Identify the blood parasite species.
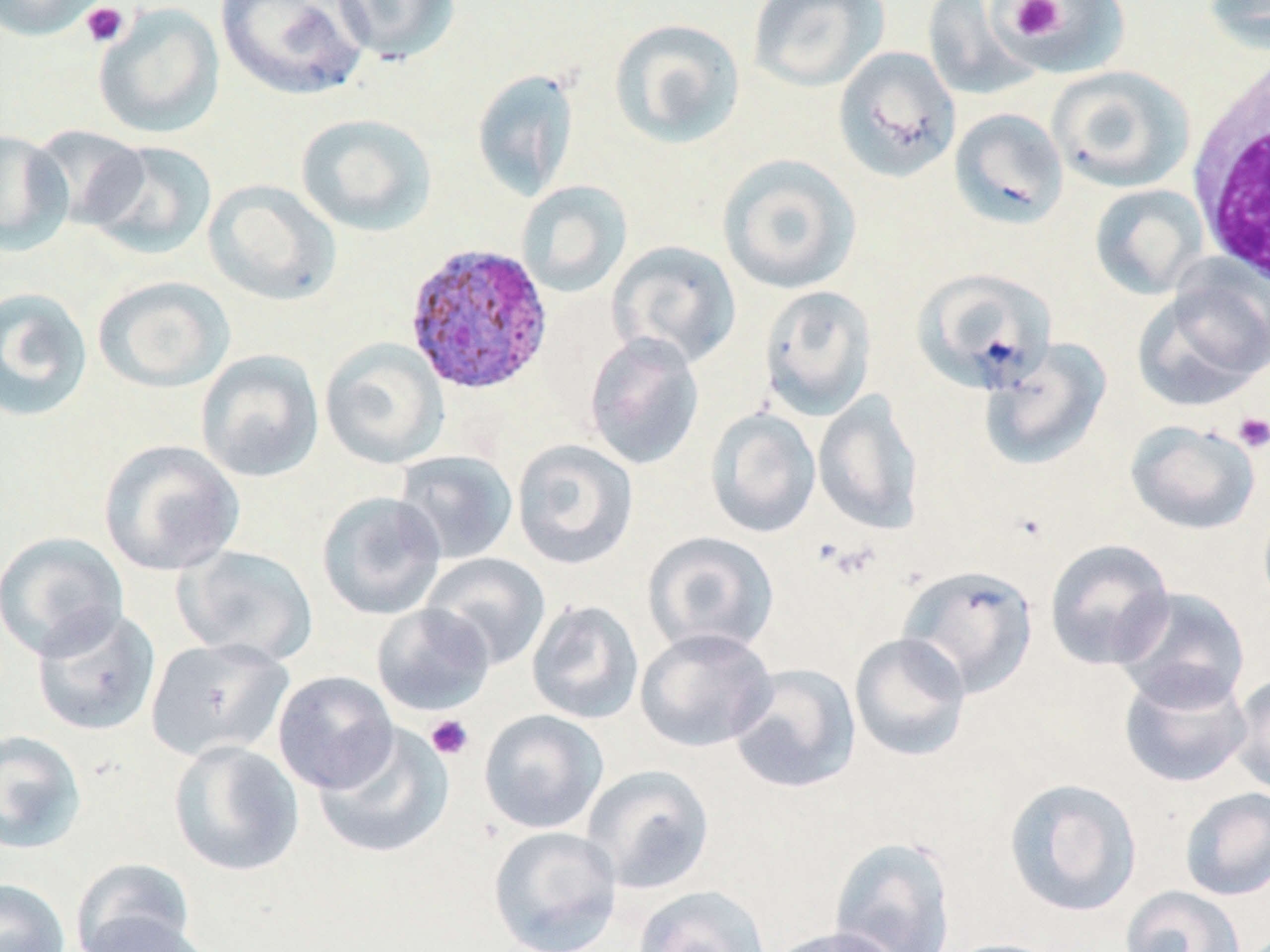

Plasmodium ovale.

Approximate bounding boxes as [x1, y1, x2, y2] in pixels. Platelet locations: [1008, 0, 1065, 41], [80, 2, 128, 47], [1233, 412, 1270, 453], [425, 714, 474, 761]. Plasmodium ovale-infected red blood cell locations: [403, 242, 554, 396]. White blood cell locations: [1186, 54, 1270, 289]. Uninfected red blood cell locations: [0, 0, 108, 42], [214, 0, 369, 102], [332, 0, 459, 65], [747, 0, 890, 93], [922, 0, 1041, 102], [1002, 0, 1129, 77], [1203, 0, 1270, 53], [93, 3, 225, 139], [608, 17, 746, 149], [832, 46, 961, 183], [1046, 65, 1195, 193], [471, 68, 579, 202], [949, 108, 1069, 229], [295, 113, 437, 236], [29, 124, 150, 231], [0, 130, 72, 255], [84, 140, 217, 261], [717, 153, 862, 295], [203, 179, 341, 306], [516, 180, 633, 298], [1089, 183, 1209, 300], [608, 240, 741, 370], [912, 268, 1055, 394], [1134, 272, 1270, 409], [93, 276, 235, 394], [758, 284, 877, 420], [0, 287, 93, 423], [583, 332, 705, 471], [319, 338, 449, 470], [979, 338, 1113, 471], [195, 349, 324, 483], [813, 391, 924, 533], [705, 407, 821, 538], [1125, 420, 1261, 535], [97, 439, 245, 577], [511, 439, 639, 570], [393, 450, 518, 565], [316, 491, 447, 620], [0, 530, 129, 661], [642, 531, 779, 657], [1044, 538, 1175, 670], [175, 544, 318, 666], [420, 552, 551, 670], [898, 564, 1039, 698], [1112, 587, 1251, 711], [525, 599, 644, 725], [370, 604, 496, 717], [31, 605, 161, 737], [635, 627, 777, 753], [849, 632, 971, 762], [145, 637, 292, 762], [728, 663, 861, 794], [1119, 668, 1252, 788], [273, 670, 398, 794], [1229, 671, 1270, 798], [478, 709, 609, 834], [313, 724, 453, 859], [0, 729, 87, 855], [168, 740, 304, 877], [582, 764, 715, 894], [1003, 777, 1142, 917], [1179, 787, 1270, 901], [487, 825, 622, 951], [829, 836, 957, 952], [70, 858, 197, 952], [0, 878, 70, 952], [631, 885, 771, 952], [1120, 885, 1246, 952], [78, 910, 215, 952], [764, 926, 905, 952], [938, 938, 1068, 952]. One field of a larger specimen. May-Grünwald-Giemsa stain. Image is 1270×952 pixels. Thin blood film. Optical microscopy. Captured at 1000x magnification.